Name the parasite shown.
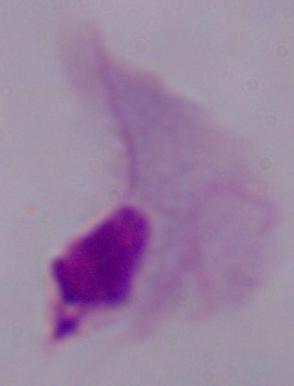
This is a trichomonad.

{
  "modality": "micrograph",
  "magnification": "1000x"
}